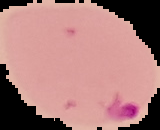

image type = segmented cell region on a black background
image size = 160×130 pixels
result = malaria parasites detected
preparation = thin blood smear